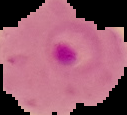

image size = 127×115 pixels
image type = cell region segmented out of the field of view; surrounding area masked to black
malaria status = parasitized
preparation = thin blood smear